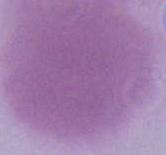

{
  "magnification": "1000x",
  "identification": "red blood cell",
  "modality": "micrograph"
}